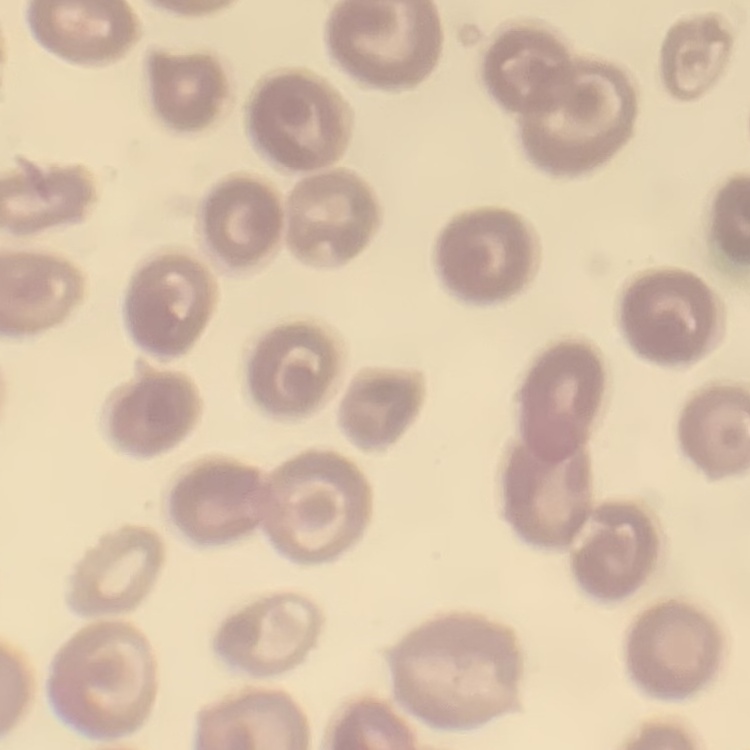

Summary:
  - Erythrocyte morphology: no rouleaux formation
  - Preparation: thin blood film
  - Stain: Field's or Giemsa
  - Image type: one tile cut from a larger photomicrograph